Identify the parasite.
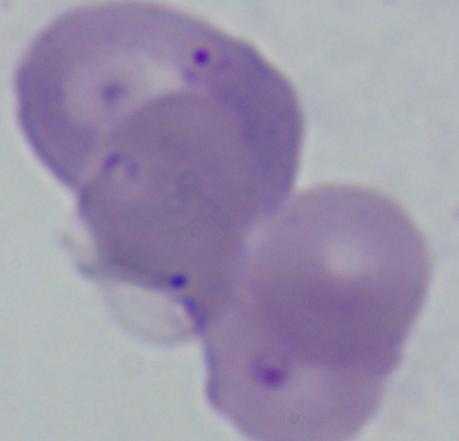

Babesia.

magnification = 1000x
modality = photomicrograph